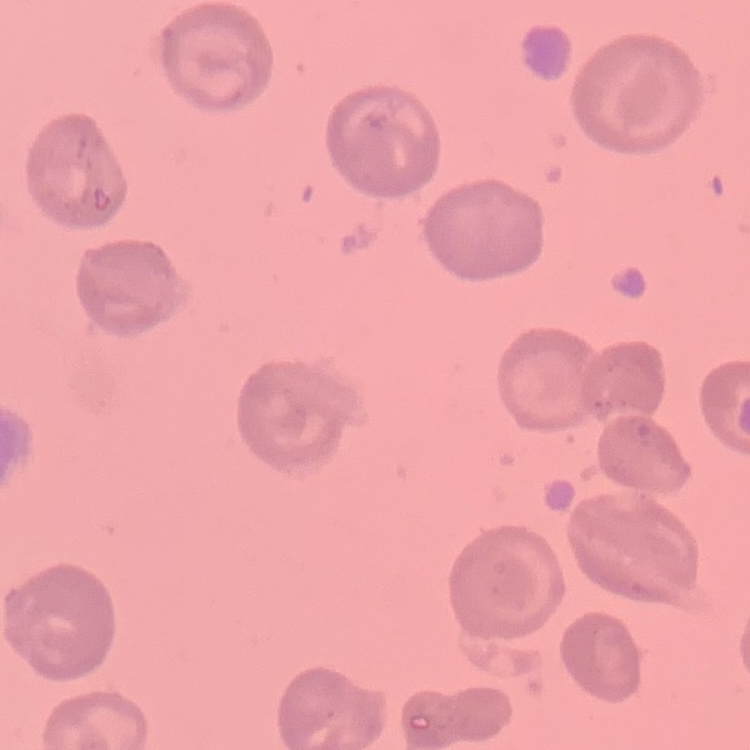
The erythrocytes show no rouleaux formation. Field's or Giemsa stain. Thin blood film. One tile cut from a larger photomicrograph.